Describe the morphology of the erythrocytes.
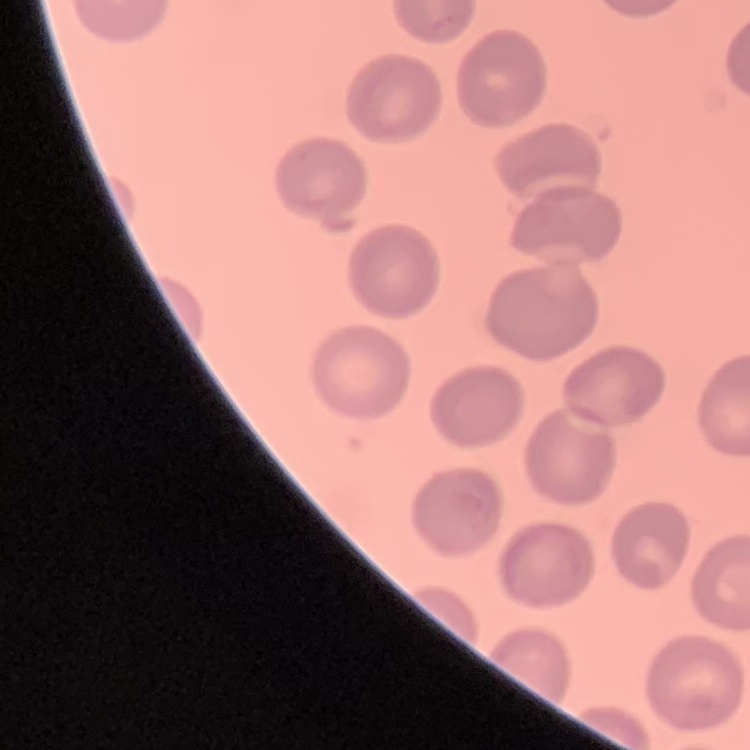
They show no rouleaux formation.

Summary:
  - Image type: square crop of a larger photomicrograph
  - Preparation: thin blood smear
  - Stain: Field's or Giemsa